Assess this cell for malaria.
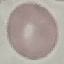
Uninfected.

Giemsa-stained preparation. Cell patch, automatically extracted from a larger field of view and resized to 64 × 64 pixels. Acquired by smartphone through the microscope eyepiece. Thin blood film.